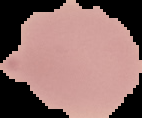

{
  "image_type": "segmented cell region with the area outside set to black",
  "image_size": "142×118 pixels",
  "preparation": "thin blood smear",
  "result": "no malaria parasites seen"
}